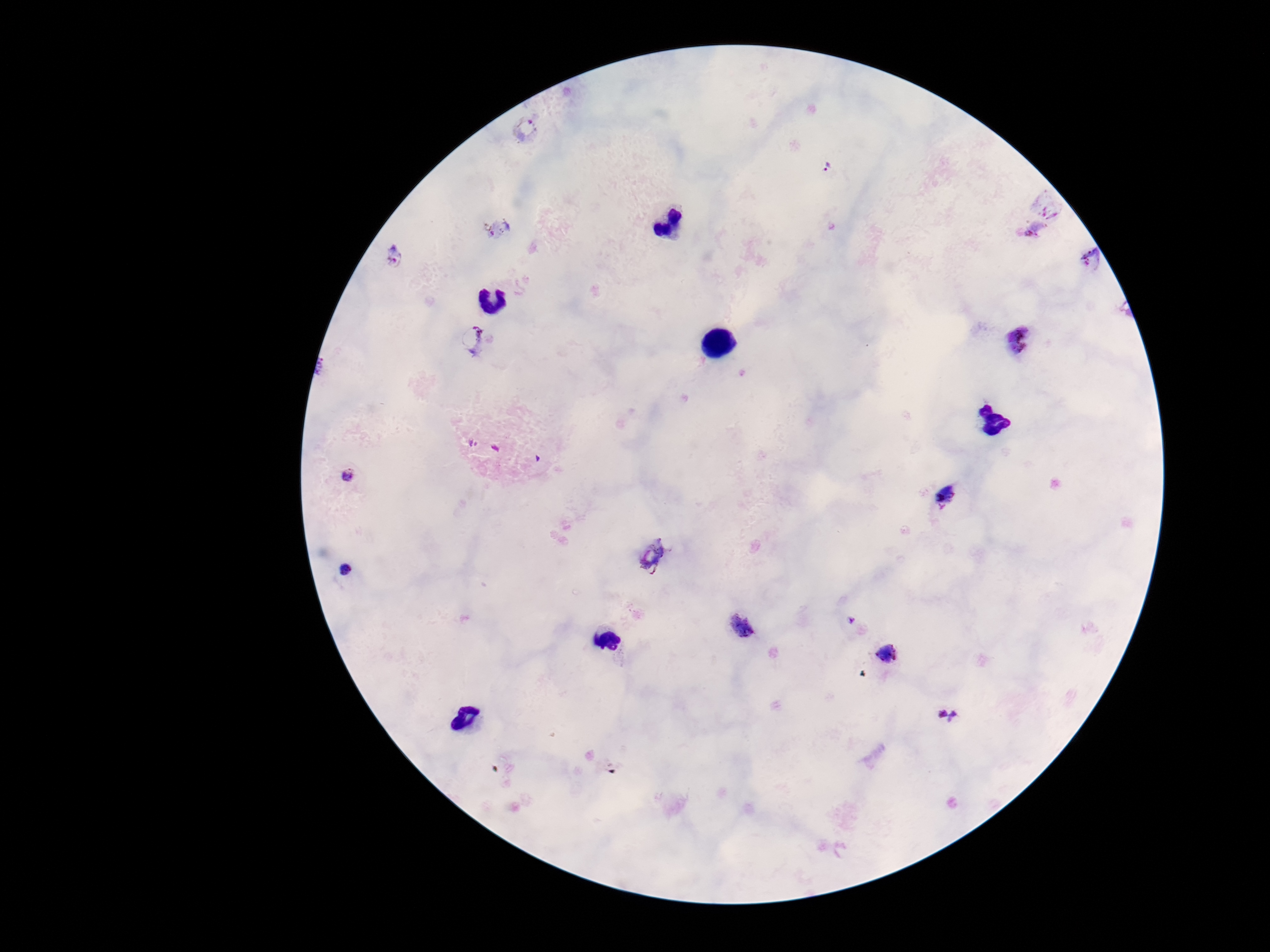
field of view = one from this slide
stain = Giemsa
Plasmodium parasite locations = approximate centers as [x, y] in pixels: [525, 129], [828, 166], [1034, 229], [502, 230], [394, 256], [1090, 258], [474, 339], [1018, 340], [348, 472], [944, 497], [652, 556], [345, 570], [851, 621], [740, 624], [610, 640], [888, 654], [947, 714]
capture = smartphone camera through the microscope eyepiece
image size = 1270×952 pixels
patient malaria status = infected
preparation = thick blood smear
magnification = 100x